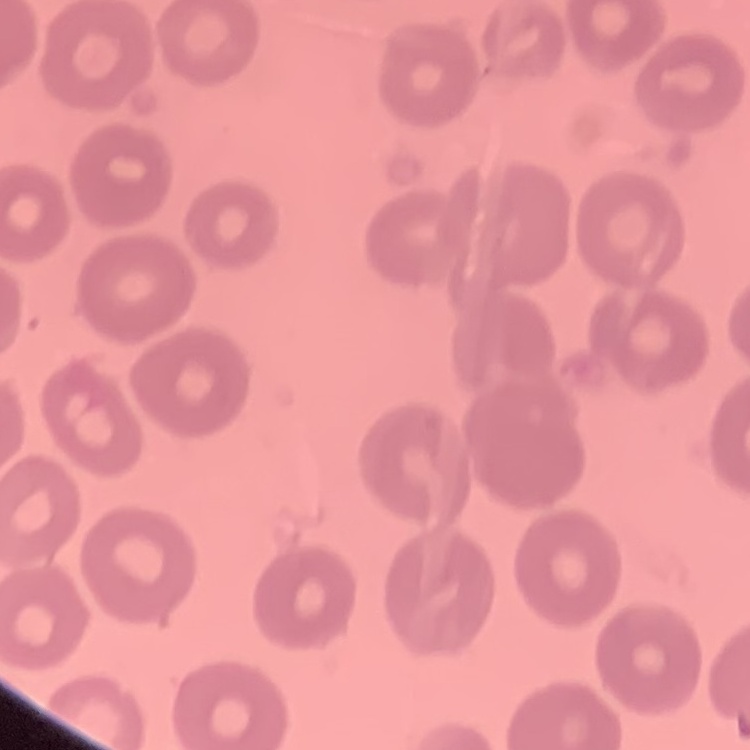
Summary:
  - Erythrocyte morphology: no rouleaux formation
  - Stain: Field's or Giemsa
  - Image type: one tile cut from a larger photomicrograph
  - Preparation: thin peripheral smear